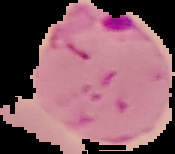 The area outside the segmented cell region is set to black. Image is 175×154 pixels. From a thin blood smear. Result: malaria parasites identified.